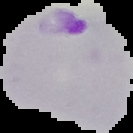

Image is 133×133 pixels. Malaria status: parasitized. Segmented cell region on a black background. From a thin blood smear.